Locate every uninfected red blood cell.
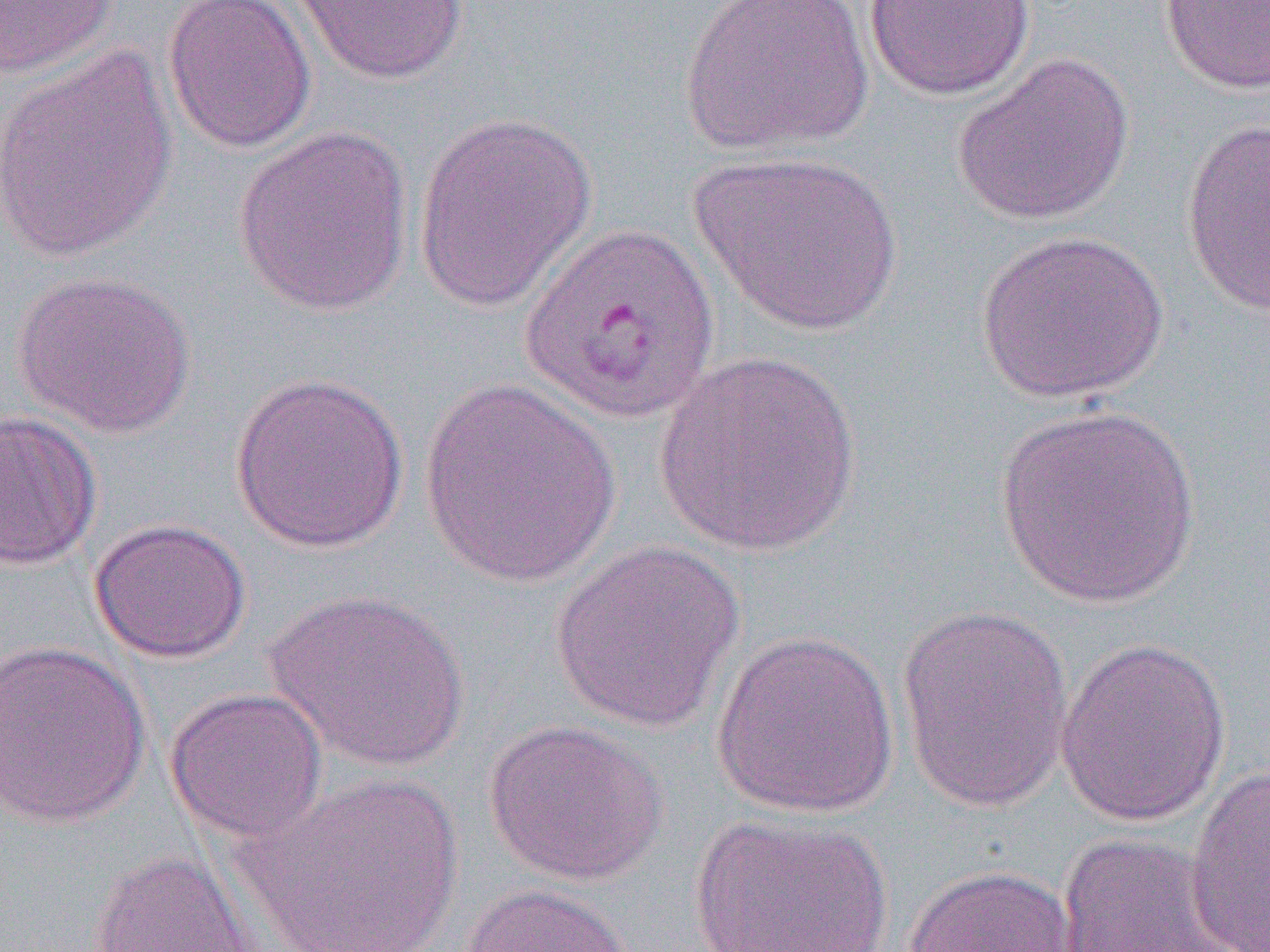
Approximate bounding boxes as (x1,y1)-(x2,y2) corner pairs in pixels.
Uninfected red blood cells: (0,0)-(119,79), (161,0)-(317,153), (291,0)-(469,85), (679,0)-(874,157), (1158,0)-(1270,95), (865,1)-(1036,101), (0,45)-(179,264), (952,52)-(1136,227), (412,111)-(598,313), (1181,118)-(1270,318), (232,124)-(414,317), (689,150)-(904,338), (976,228)-(1169,403), (12,269)-(196,439), (652,350)-(862,556), (230,370)-(410,554), (419,378)-(621,589), (994,404)-(1203,609), (0,410)-(103,571), (88,518)-(252,663), (548,541)-(746,733), (264,589)-(470,771), (895,604)-(1075,815), (711,629)-(900,818), (1056,635)-(1231,826), (0,639)-(151,828), (164,687)-(329,845), (483,718)-(668,887), (1184,763)-(1270,952), (238,770)-(465,951), (686,813)-(895,951), (1053,833)-(1251,952), (87,849)-(262,952), (903,864)-(1080,952), (459,882)-(638,952).

{
  "slide_level_diagnosis": "Plasmodium vivax",
  "image_size": "1270×952 pixels",
  "magnification": "1000x",
  "preparation": "thin blood film",
  "modality": "optical microscopy",
  "field_of_view": "single"
}